Classify this cell by malaria status.
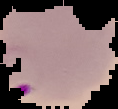

Parasitized.

Summary:
  - Image size: 118×109 pixels
  - Image type: segmented cell region on a black background
  - Preparation: thin blood smear